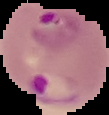

From a thin blood smear. Malaria status: parasitized. Segmented cell region on a black background. Image is 109×115 pixels.